Point out each malaria parasite and each leukocyte.
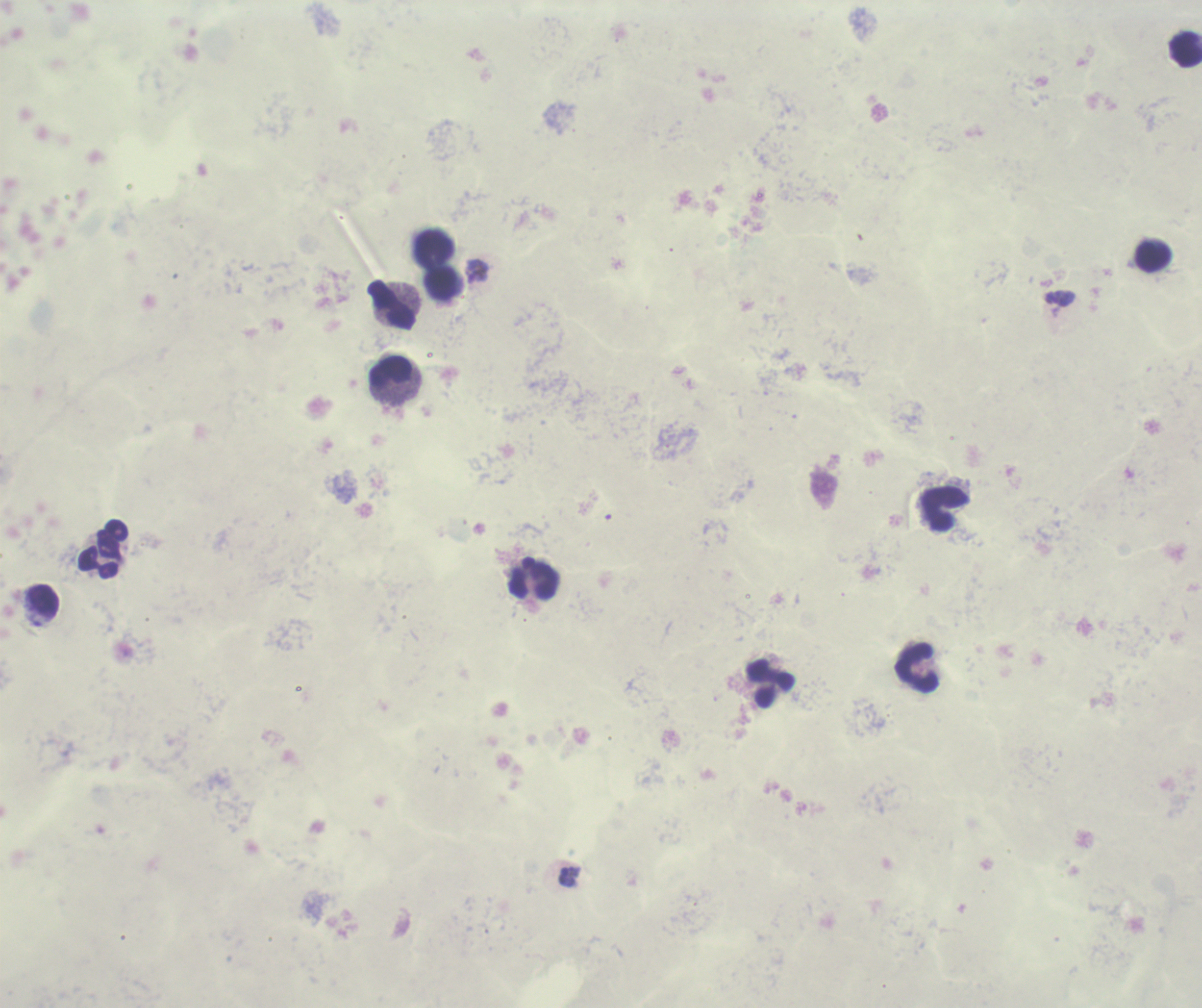

Approximate centers as (x, y) in pixels.
Trophozoites: (477, 271), (570, 877).
No schizont or gametocyte forms observed.
Leukocytes: (1185, 50), (436, 247), (1153, 257), (441, 285), (393, 305), (391, 371), (944, 509), (98, 554), (535, 581), (43, 600), (917, 667), (772, 684).

Image is 1202×1008 pixels. Coloration quality: bad. One field from this slide. Previously used in an actual diagnosis. Captured at 100x magnification. Background quality: unsatisfactory. Romanowsky stain. Thick smear of blood.